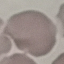 Malaria status: uninfected. Automatically extracted cell patch, resized to 64 × 64 pixels. Photographed with a smartphone camera at the microscope eyepiece. Thin blood film. Giemsa stain.